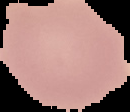

preparation = thin blood smear
image size = 130×112 pixels
image type = segmented cell region with the area outside set to black
malaria status = uninfected